Locate and identify every blood parasite.
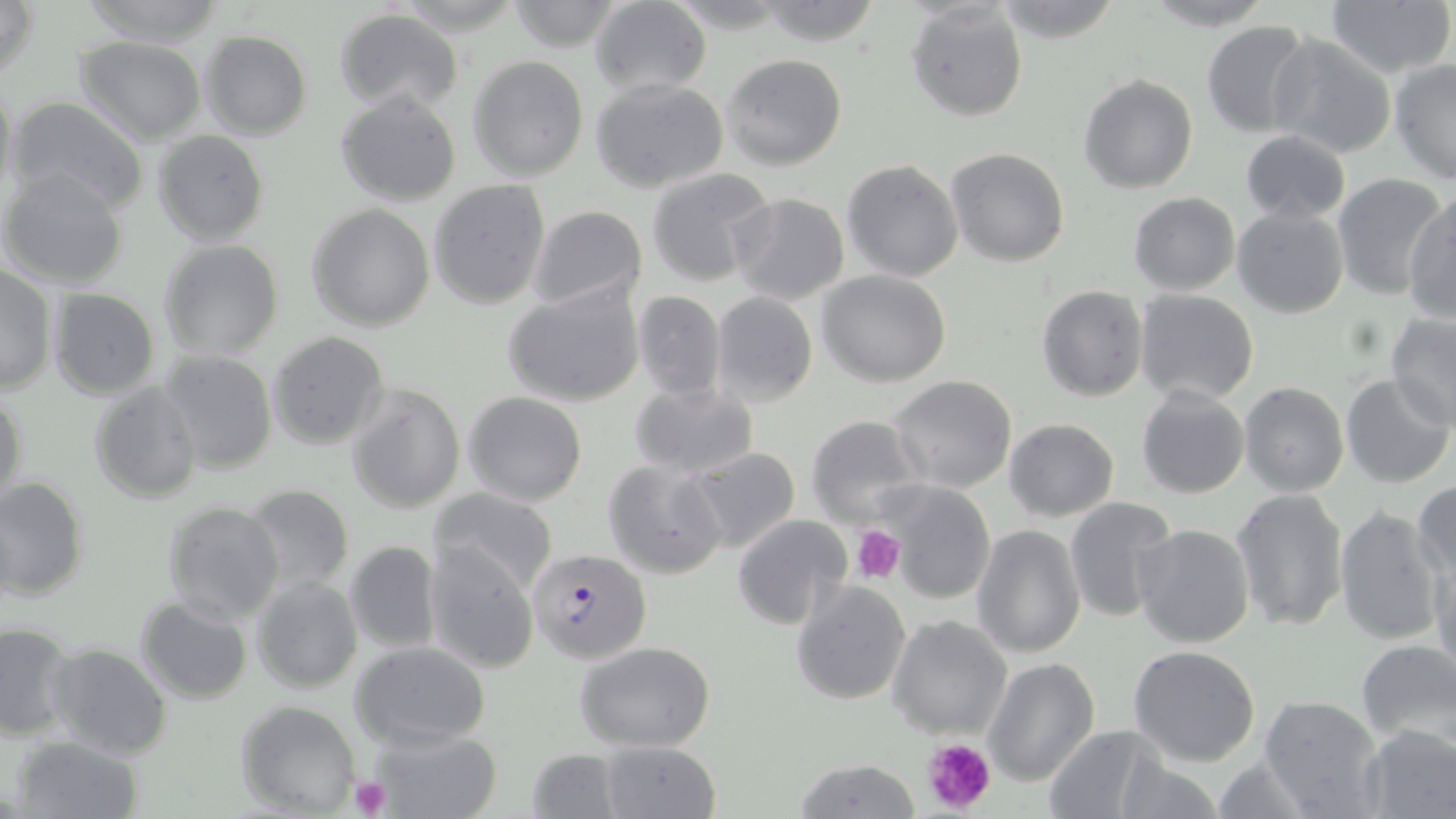

Approximate bounding boxes as [x1, y1, x2, y2] in pixels.
Plasmodium falciparum-infected red blood cells: [528, 547, 652, 664].
No Plasmodium ovale, Plasmodium malariae, Plasmodium vivax, Babesia divergens, or Trypanosoma brucei observed.

Uninfected red blood cell locations: [1, 0, 39, 84], [76, 0, 226, 47], [753, 0, 883, 45], [993, 0, 1126, 45], [1140, 0, 1278, 30], [503, 1, 626, 51], [588, 1, 713, 96], [1324, 1, 1454, 80], [906, 3, 1029, 122], [332, 7, 464, 116], [1201, 21, 1313, 137], [198, 29, 313, 139], [1267, 34, 1396, 159], [74, 37, 208, 146], [721, 53, 849, 171], [467, 55, 589, 181], [1390, 59, 1456, 183], [1078, 73, 1199, 193], [590, 76, 729, 194], [0, 77, 19, 212], [336, 91, 461, 206], [4, 97, 152, 215], [152, 129, 269, 246], [1239, 129, 1350, 224], [946, 147, 1070, 266], [842, 159, 963, 282], [0, 166, 130, 289], [645, 168, 775, 286], [1331, 174, 1447, 298], [428, 180, 550, 310], [1403, 191, 1456, 323], [729, 192, 850, 308], [1127, 192, 1240, 296], [307, 203, 436, 331], [526, 204, 648, 314], [1232, 206, 1349, 318], [159, 238, 285, 360], [0, 264, 57, 395], [817, 269, 953, 387], [503, 282, 645, 408], [1036, 284, 1150, 402], [48, 288, 161, 399], [631, 290, 726, 400], [710, 291, 818, 406], [1133, 291, 1259, 407], [1385, 312, 1456, 428], [266, 331, 391, 450], [157, 351, 278, 475], [889, 374, 1018, 493], [1340, 374, 1453, 488], [89, 378, 203, 504], [629, 379, 758, 480], [345, 383, 466, 515], [1239, 383, 1349, 498], [1135, 385, 1249, 499], [0, 389, 27, 515], [462, 390, 588, 506], [804, 414, 927, 528], [1005, 418, 1119, 520], [684, 447, 801, 555], [602, 457, 729, 581], [0, 477, 90, 603], [1411, 479, 1455, 588], [881, 482, 997, 605], [242, 484, 354, 595], [430, 487, 557, 597], [1231, 487, 1349, 632], [1064, 496, 1178, 622], [163, 501, 285, 626], [1334, 506, 1447, 648], [733, 514, 853, 628], [1132, 522, 1255, 649], [972, 523, 1086, 658], [1428, 540, 1455, 685], [343, 541, 441, 654], [424, 543, 538, 672], [251, 576, 362, 692], [789, 579, 911, 703], [136, 596, 254, 705], [887, 615, 1013, 740], [0, 623, 75, 740], [351, 640, 492, 749], [1356, 640, 1456, 751], [574, 641, 717, 750], [44, 643, 172, 759], [1128, 644, 1261, 767], [984, 658, 1099, 788], [1259, 695, 1385, 819], [235, 699, 364, 817], [1042, 724, 1169, 818], [1357, 724, 1456, 818], [365, 726, 502, 819], [10, 735, 145, 819], [596, 739, 722, 819], [524, 747, 626, 817], [1111, 748, 1226, 819], [791, 757, 922, 818], [1209, 757, 1318, 816]. Platelet locations: [852, 526, 907, 583], [921, 737, 997, 815], [351, 776, 389, 818]. Slide-level diagnosis: Plasmodium falciparum. Captured at 1000x magnification. Thin blood smear. Image is 1456×819 pixels. May-Grünwald-Giemsa-stained preparation. Single field of view. Optical microscopy.